Locate every Plasmodium falciparum parasite and give its life-cycle stage, and locate every leukocyte and any debris.
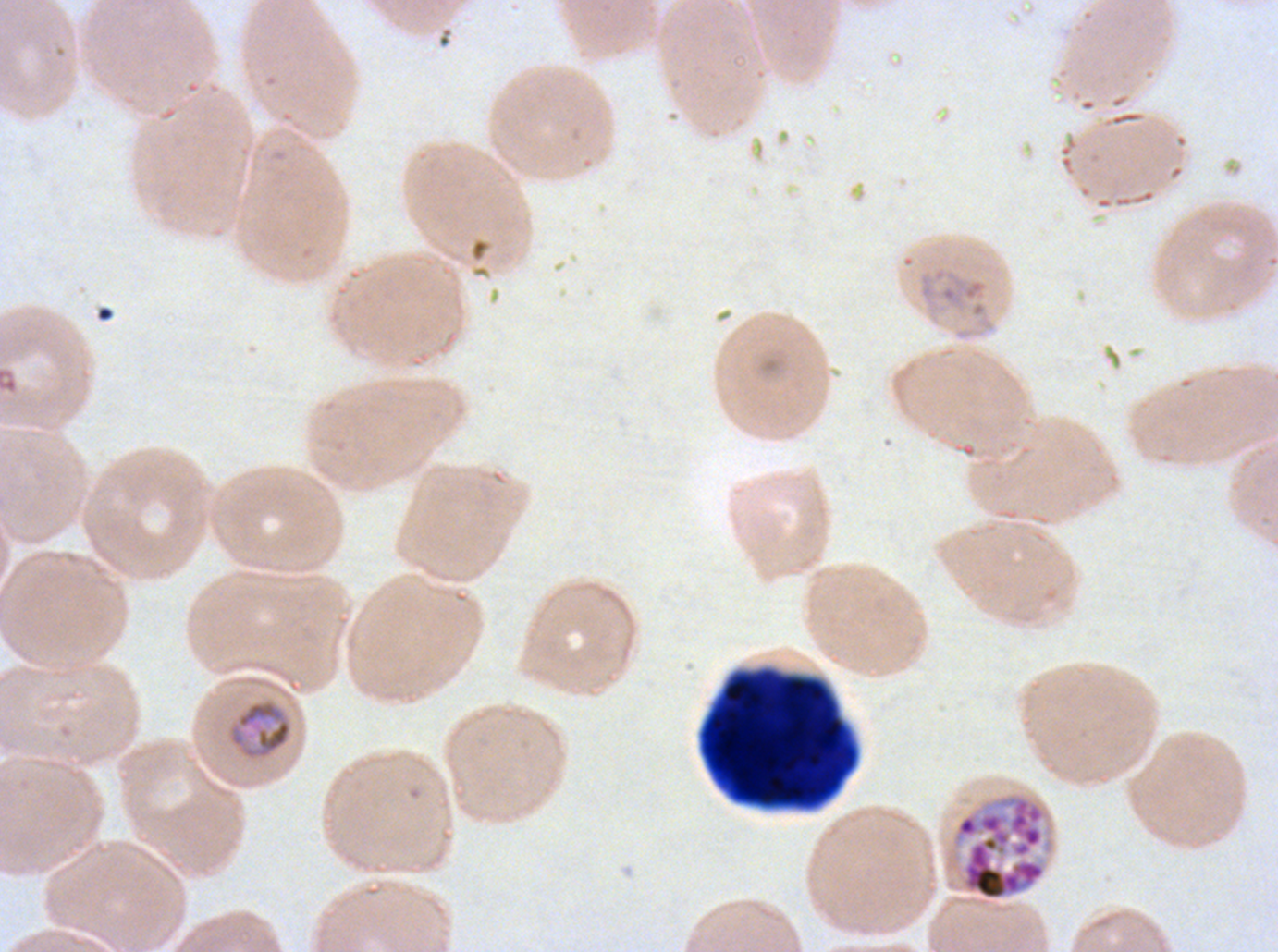
Approximate bounding boxes as [x1, y1, x2, y2] in pixels.
Mid trophozoites: [227, 699, 292, 760].
Late schizonts: [950, 791, 1055, 902].
Debris: [701, 674, 855, 805].
No rings, late-ring/early-trophozoite forms, late trophozoites, early schizonts, segmenters, gametocytes, or leukocytes observed.

field of view = one sub-image of a larger composite
stain = Giemsa
specimen = Plasmodium falciparum cultured ex vivo for 24 to 48 hours, from a patient in The Gambia
image size = 1278×952 pixels
life-cycle stages observed = mid trophozoite, late schizont
preparation = thin blood film